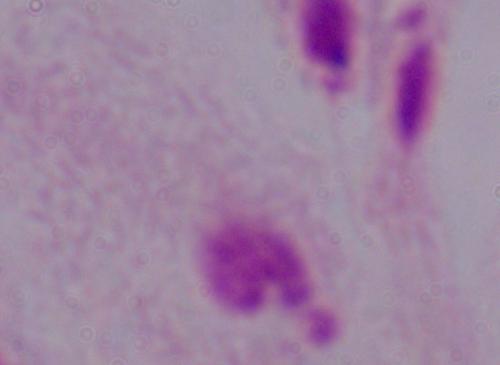
Captured at 1000x magnification. A trichomonad is seen. Micrograph.